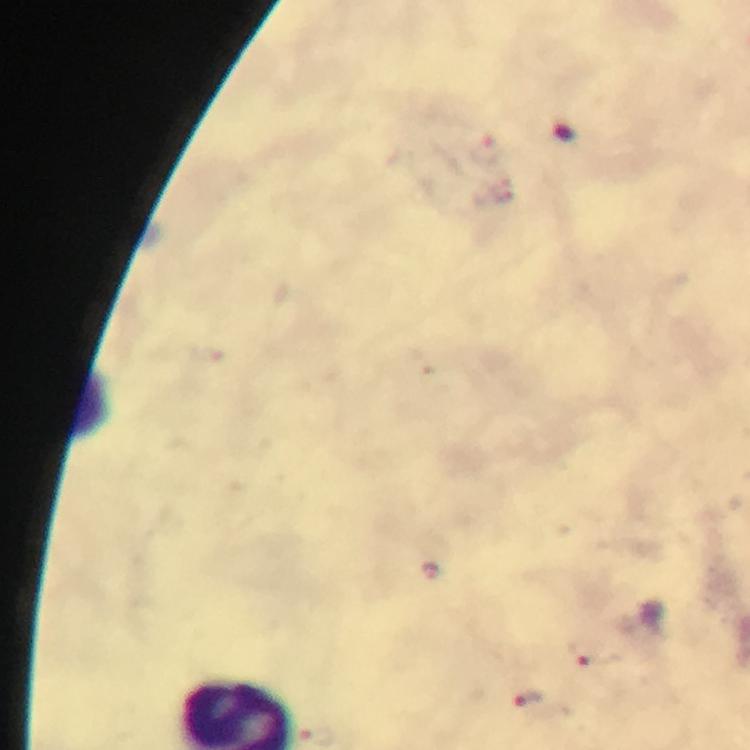

Approximate centers as {x, y} in pixels. Malaria parasite locations: {487, 150}, {586, 655}, {524, 700}. Immersion oil applied. Photographed with a smartphone mounted on the microscope. Giemsa stain. From a malaria diagnostic workup. At 100x magnification. Image is 750×750 pixels. Cropped region of a single field of view. Thick smear.